Look for Plasmodium parasites.
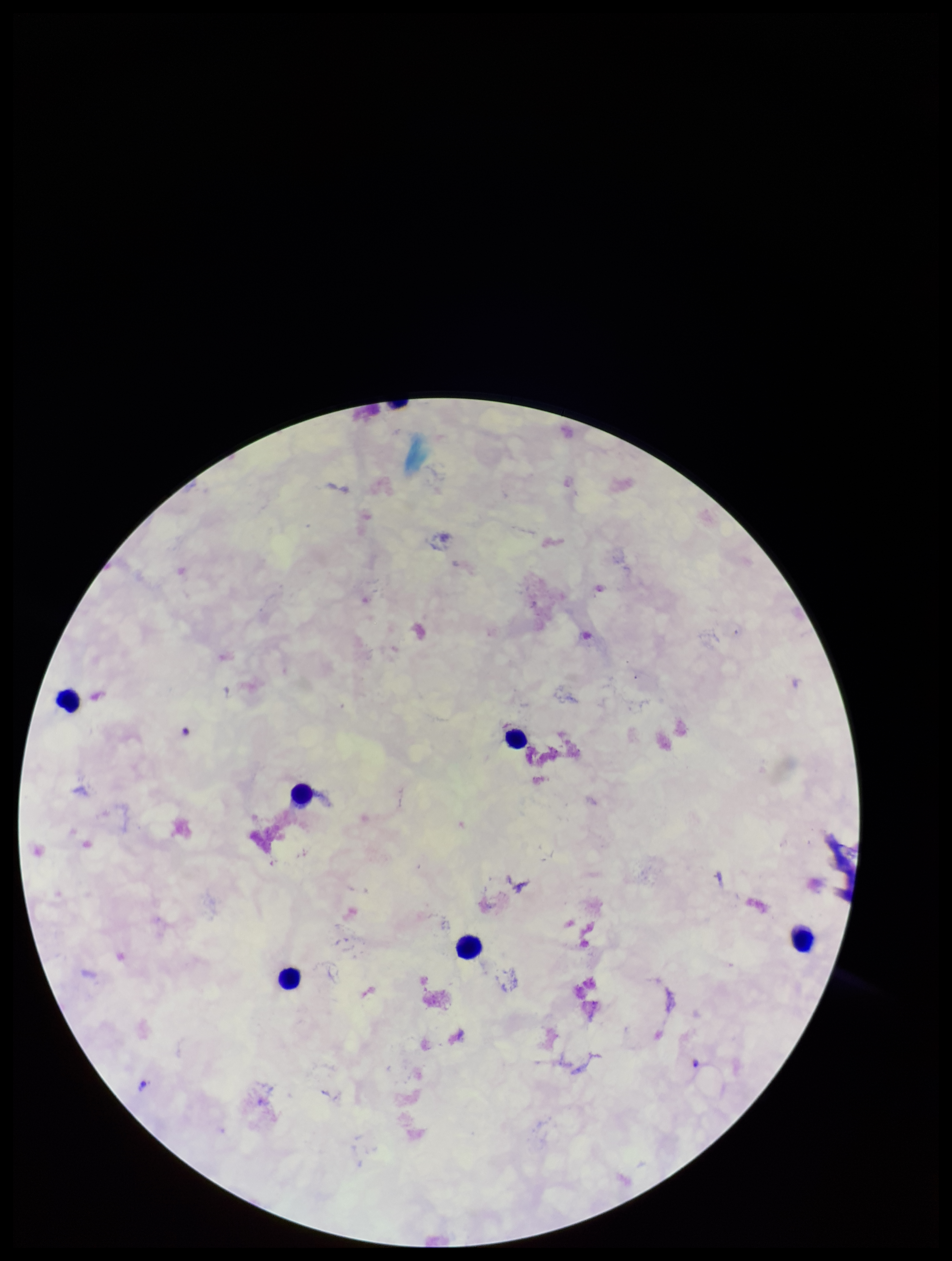

Seen.

Patient malaria status: infected. Single field of view. Leukocyte count: 6. Image is 952×1261 pixels. Species reported for this patient: Plasmodium falciparum. Smartphone photograph taken through the eyepiece of a microscope. Preparation: thick smear. Parasite count: 1. Stained with Giemsa.